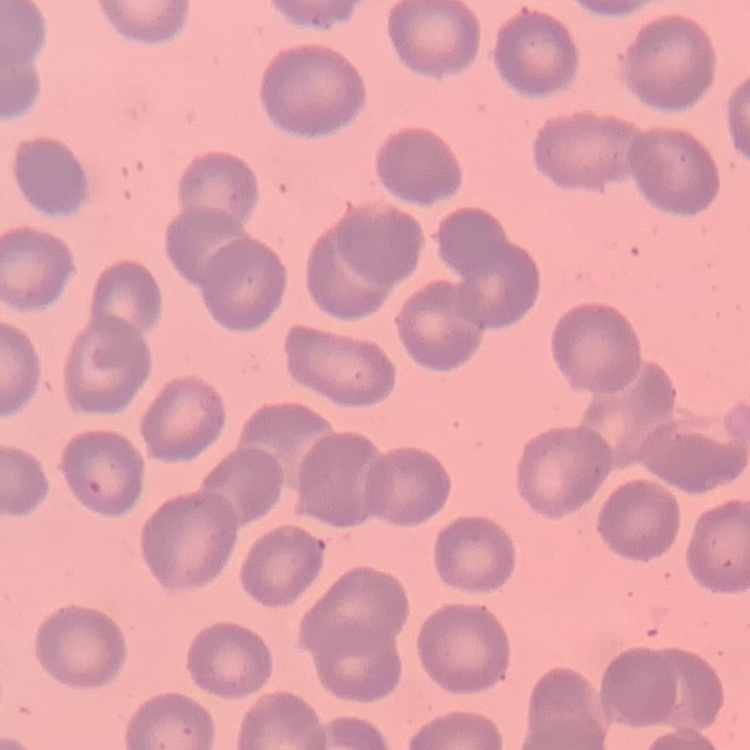

erythrocyte morphology = no rouleaux formation
preparation = thin blood film
stain = Field's or Giemsa
image type = one tile cut from a larger photomicrograph